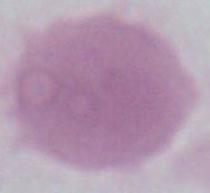

magnification = 1000x
modality = photomicrograph
identification = erythrocyte